Locate every Babesia divergens-infected red blood cell.
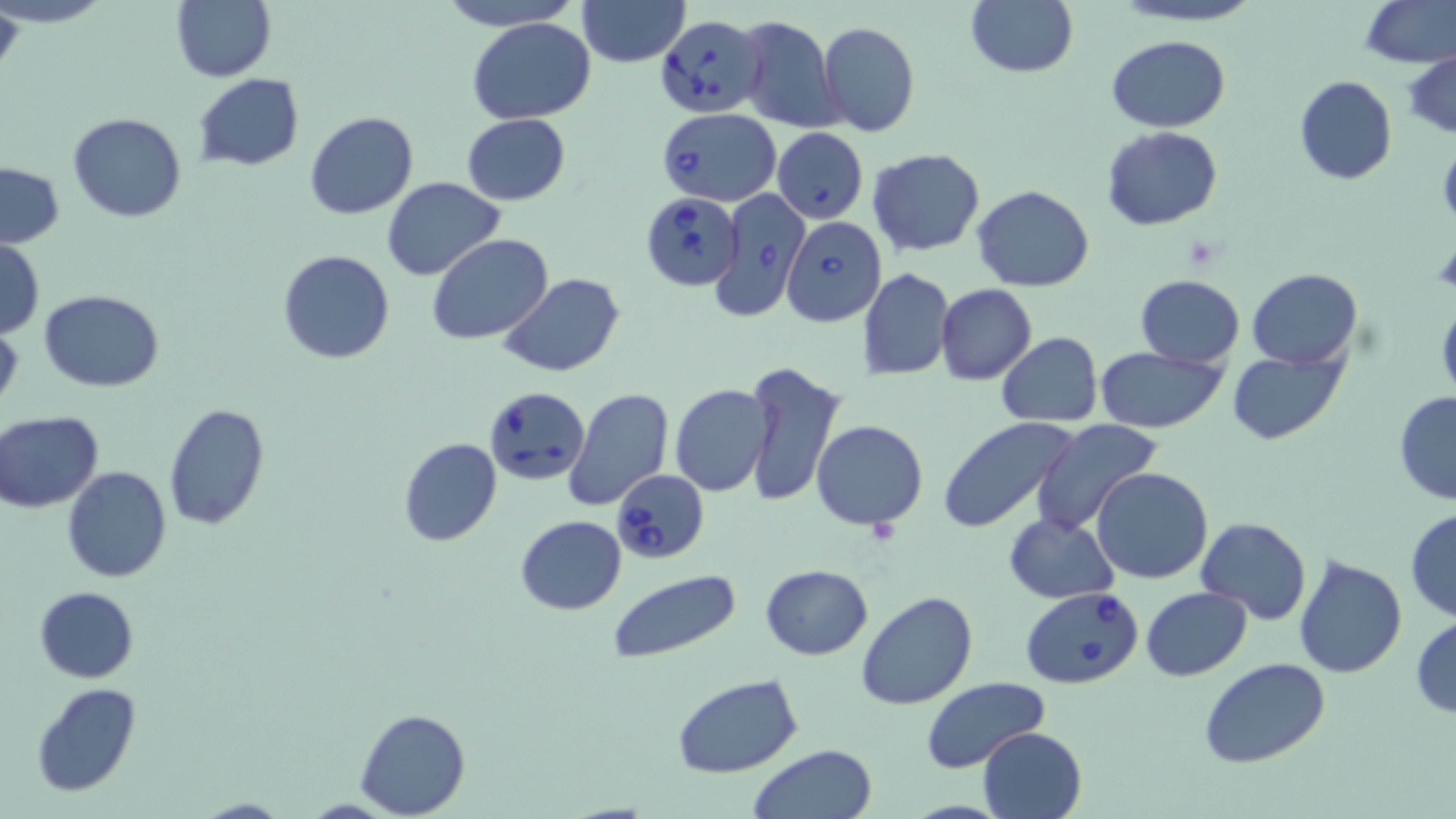

Approximate bounding boxes as [x1, y1, x2, y2] in pixels.
Babesia divergens-infected red blood cells: [655, 14, 767, 117], [657, 108, 782, 205], [771, 127, 867, 224], [709, 187, 812, 317], [639, 191, 743, 291], [780, 216, 887, 326], [482, 385, 590, 488], [611, 468, 709, 563], [1019, 586, 1143, 688].

Summary:
  - Uninfected red blood cell locations: [0, 0, 24, 83], [171, 0, 276, 83], [433, 0, 583, 28], [575, 0, 689, 67], [966, 0, 1077, 77], [1110, 0, 1268, 27], [1360, 0, 1455, 68], [468, 17, 595, 125], [736, 17, 843, 132], [817, 22, 919, 137], [1106, 34, 1231, 132], [1404, 51, 1456, 139], [194, 75, 304, 170], [1295, 75, 1396, 185], [304, 111, 417, 220], [67, 112, 188, 222], [461, 113, 571, 205], [1100, 125, 1223, 231], [867, 147, 984, 257], [0, 162, 65, 248], [380, 177, 504, 281], [972, 183, 1093, 292], [427, 234, 552, 345], [1, 239, 45, 337], [276, 249, 396, 363], [1246, 267, 1362, 368], [860, 268, 953, 380], [499, 273, 623, 377], [1136, 273, 1244, 369], [937, 284, 1037, 384], [40, 290, 164, 392], [1436, 301, 1456, 403], [0, 322, 23, 415], [996, 332, 1104, 427], [1094, 345, 1229, 434], [1228, 349, 1348, 443], [742, 361, 845, 508], [670, 385, 771, 496], [563, 387, 673, 510], [1394, 391, 1456, 505], [162, 403, 270, 531], [1, 412, 103, 513], [938, 415, 1080, 534], [1030, 418, 1163, 535], [811, 420, 927, 530], [398, 437, 502, 547], [62, 467, 171, 583], [1092, 467, 1213, 584], [1405, 507, 1456, 621], [1005, 512, 1118, 603], [515, 515, 627, 615], [1195, 516, 1312, 623], [1294, 553, 1408, 679], [761, 564, 873, 660], [608, 571, 741, 665], [34, 585, 139, 683], [1141, 586, 1251, 680], [857, 592, 979, 711], [1410, 614, 1456, 720], [1198, 656, 1331, 769], [672, 674, 804, 779], [920, 677, 1049, 775], [29, 683, 141, 799], [356, 708, 470, 818], [978, 725, 1089, 819], [749, 743, 878, 819], [193, 798, 293, 818]
  - Slide-level diagnosis: Babesia divergens
  - Magnification: 1000x
  - Preparation: thin blood smear
  - Stain: May-Grünwald-Giemsa
  - Modality: light microscopy
  - Image size: 1456×819 pixels
  - Field of view: single